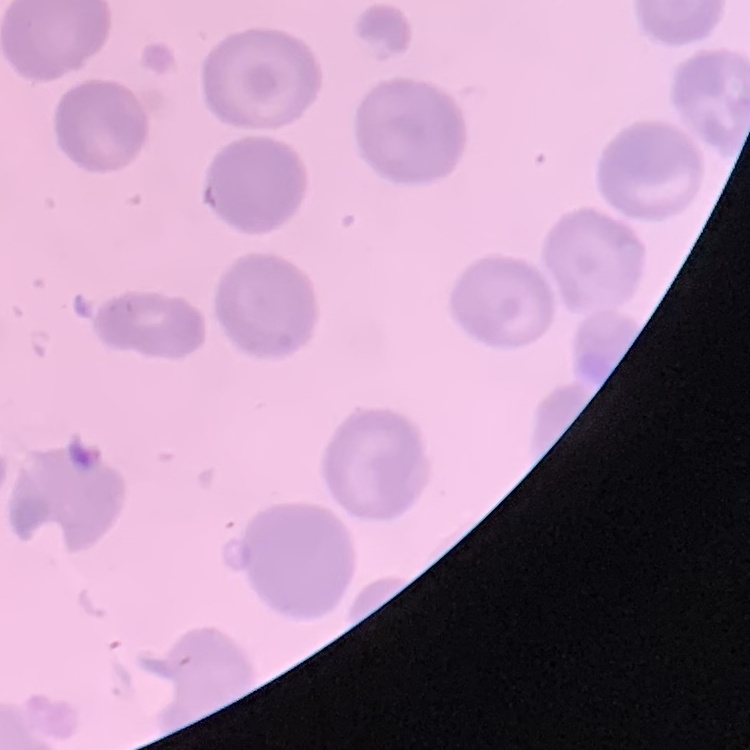
Summary:
  - Red blood cell morphology: no rouleaux formation
  - Preparation: thin blood film
  - Stain: Field's or Giemsa
  - Image type: one tile cut from a larger photomicrograph